Assess this cell for malaria.
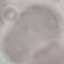

It is uninfected.

{
  "image_type": "automatically extracted cell patch, resized to 64 × 64 pixels",
  "capture": "smartphone through the microscope eyepiece",
  "stain": "Giemsa",
  "preparation": "thin blood smear"
}